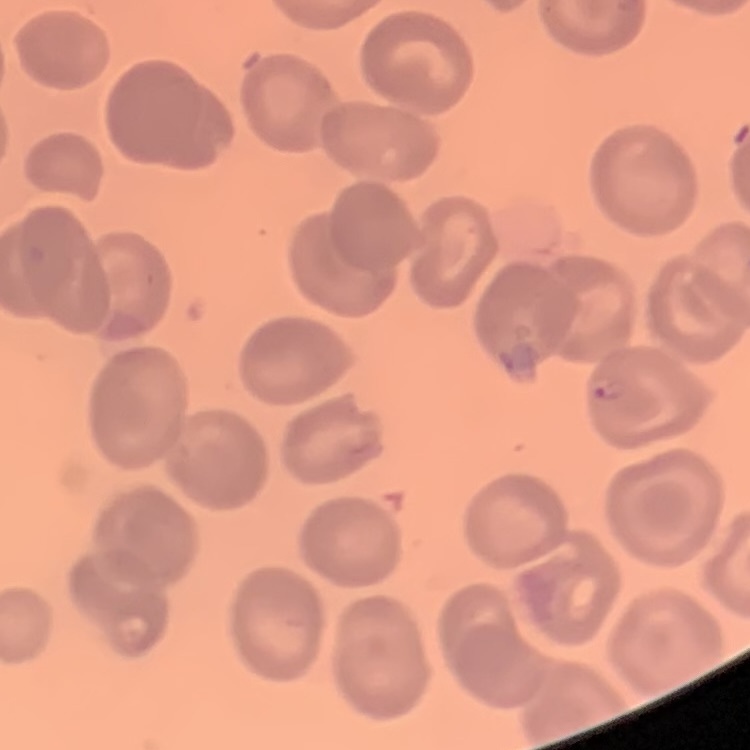
The red blood cells show no rouleaux formation. Thin blood film. Stained with either Field's or Giemsa. One tile cut from a larger photomicrograph.